Identify the parasite.
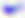
This is Toxoplasma gondii.

400x magnification. Micrograph.